Classify this cell by malaria status.
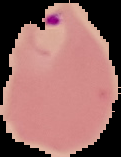
It is parasitized.

{
  "preparation": "thin blood smear",
  "image_type": "cell region segmented out of the field of view; surrounding area masked to black",
  "image_size": "121×157 pixels"
}